Locate every malaria parasite by life-cycle stage, and every leukocyte.
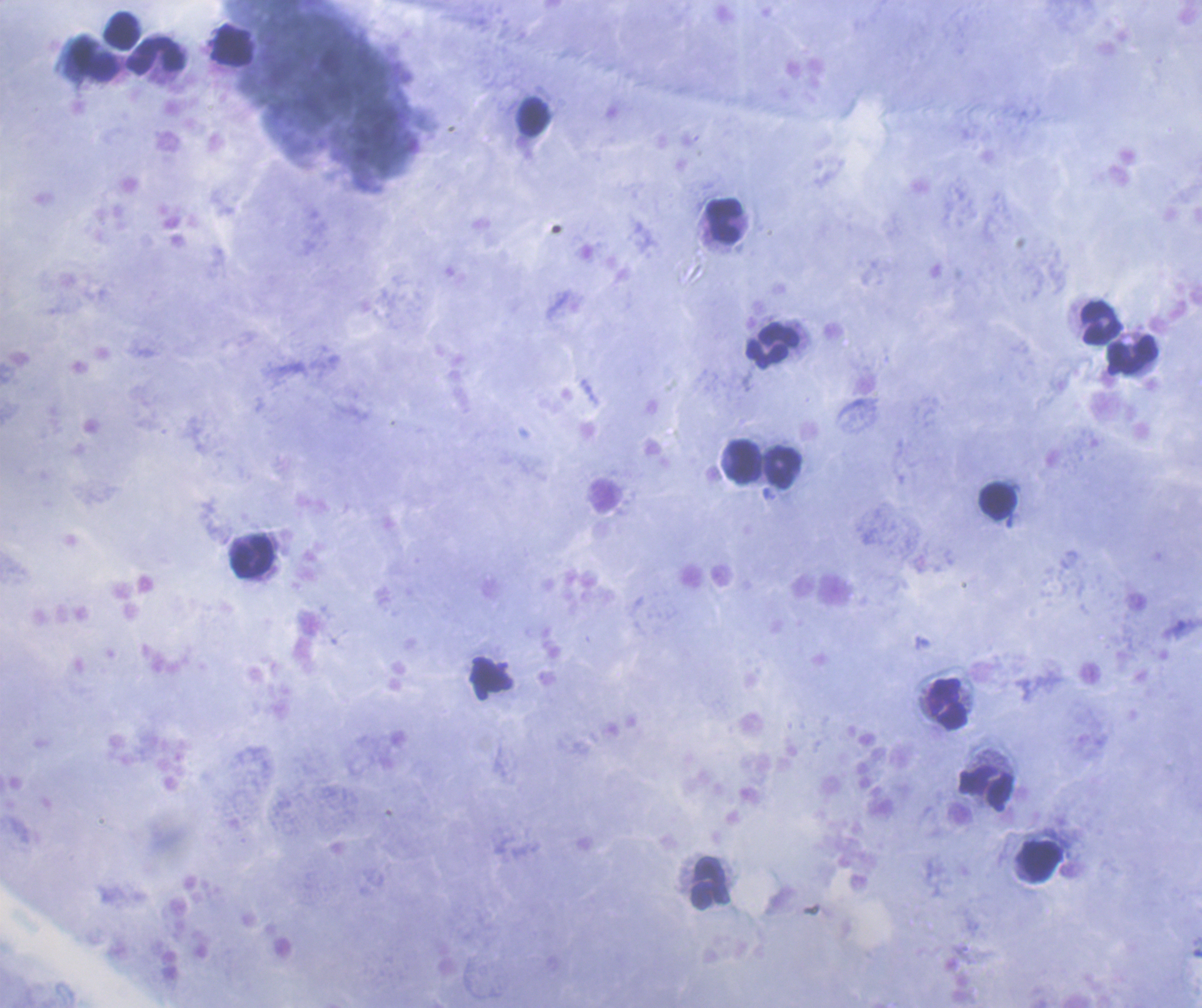

No malaria parasites detected.
Approximate centers as {x, y} in pixels.
Leukocytes: {121, 30}, {231, 45}, {156, 56}, {532, 118}, {724, 220}, {1101, 323}, {773, 346}, {1133, 354}, {742, 462}, {782, 467}, {998, 500}, {252, 556}, {492, 679}, {948, 704}, {987, 789}, {1041, 862}, {710, 883}.

field of view = single
image size = 1202×1008 pixels
coloration quality = good
stain = Romanowsky
background quality = good
context = previously used in an actual diagnosis
magnification = 100x
preparation = thick smear of blood